Locate and identify every blood parasite.
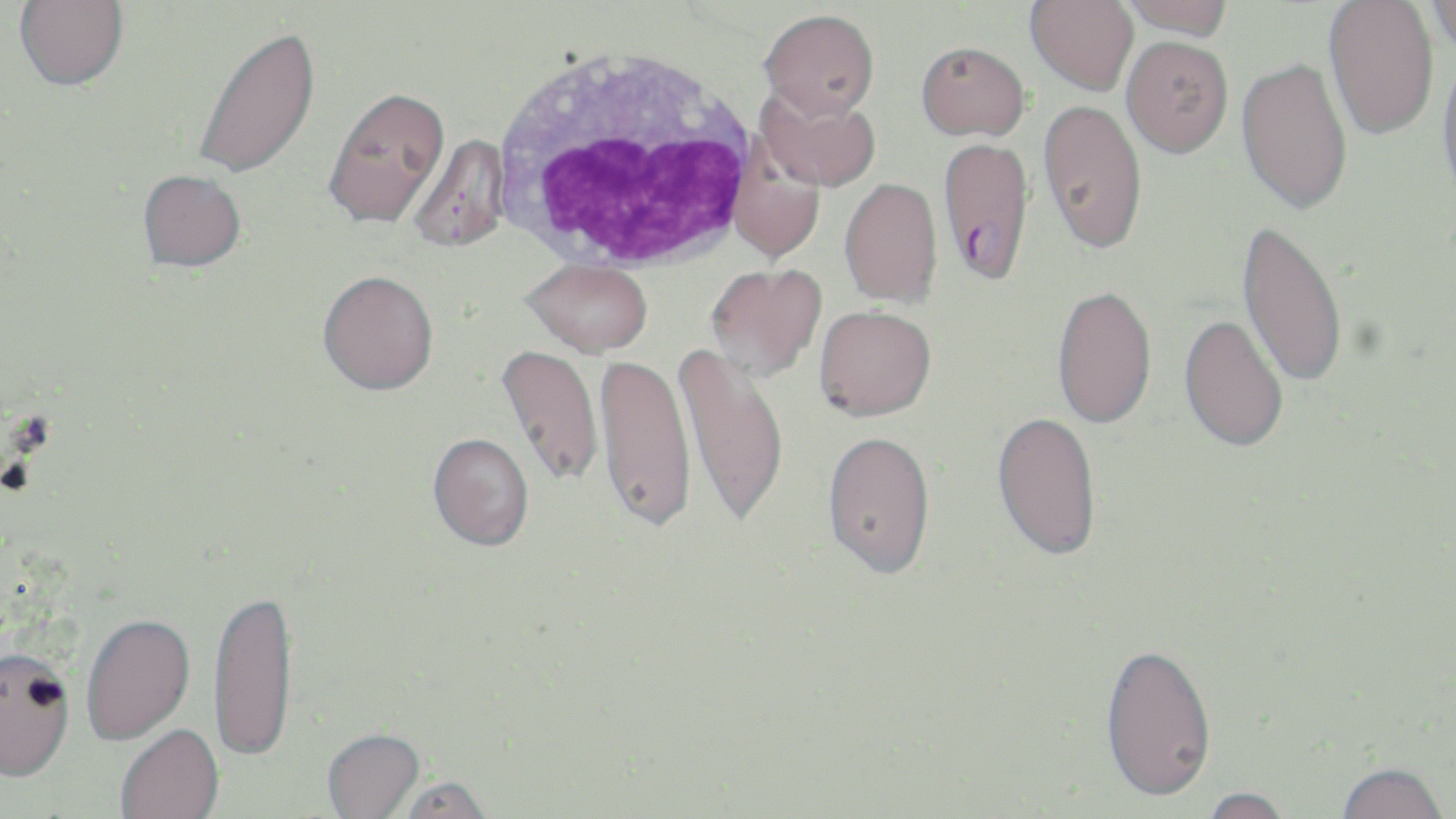

Approximate bounding boxes as named x1/y1/x2/y2 corners in pixels.
Plasmodium falciparum-infected red blood cells: (x1=937, y1=137, x2=1034, y2=285).
No Plasmodium ovale, Plasmodium malariae, Plasmodium vivax, Babesia divergens, or Trypanosoma brucei observed.

Summary:
  - White blood cell locations: (x1=490, y1=42, x2=765, y2=275)
  - Uninfected red blood cell locations: (x1=14, y1=0, x2=129, y2=90), (x1=1025, y1=0, x2=1139, y2=95), (x1=1117, y1=0, x2=1232, y2=40), (x1=1323, y1=0, x2=1440, y2=141), (x1=1423, y1=1, x2=1456, y2=56), (x1=759, y1=9, x2=879, y2=119), (x1=192, y1=24, x2=321, y2=180), (x1=1121, y1=35, x2=1233, y2=158), (x1=916, y1=41, x2=1029, y2=140), (x1=1436, y1=47, x2=1456, y2=206), (x1=1236, y1=56, x2=1354, y2=215), (x1=756, y1=84, x2=881, y2=192), (x1=323, y1=86, x2=450, y2=229), (x1=1038, y1=98, x2=1147, y2=255), (x1=406, y1=134, x2=511, y2=254), (x1=727, y1=146, x2=825, y2=264), (x1=137, y1=169, x2=246, y2=272), (x1=839, y1=177, x2=942, y2=307), (x1=1237, y1=218, x2=1349, y2=390), (x1=523, y1=258, x2=653, y2=356), (x1=704, y1=263, x2=826, y2=382), (x1=317, y1=270, x2=439, y2=394), (x1=1051, y1=285, x2=1157, y2=429), (x1=814, y1=304, x2=936, y2=420), (x1=1178, y1=313, x2=1289, y2=453), (x1=673, y1=341, x2=790, y2=529), (x1=496, y1=344, x2=604, y2=488), (x1=594, y1=352, x2=696, y2=534), (x1=992, y1=410, x2=1102, y2=561), (x1=822, y1=430, x2=936, y2=578), (x1=427, y1=433, x2=534, y2=552), (x1=209, y1=592, x2=298, y2=769), (x1=82, y1=616, x2=196, y2=748), (x1=1098, y1=641, x2=1216, y2=803), (x1=0, y1=654, x2=75, y2=787), (x1=116, y1=726, x2=224, y2=819), (x1=322, y1=730, x2=426, y2=819), (x1=1334, y1=762, x2=1449, y2=819), (x1=396, y1=777, x2=495, y2=819), (x1=1199, y1=786, x2=1296, y2=819)
  - Slide-level diagnosis: Plasmodium falciparum
  - Stain: May-Grünwald-Giemsa
  - Preparation: thin blood film
  - Magnification: 1000x
  - Image size: 1456×819 pixels
  - Field of view: one of a larger specimen
  - Modality: light microscopy